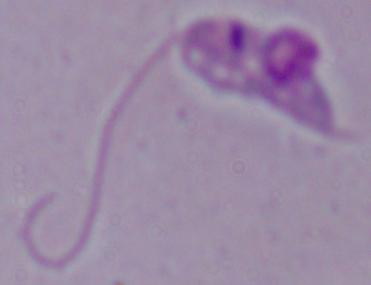

1000x magnification. A Leishmania parasite is shown. Micrograph.